Describe the morphology of the red blood cells.
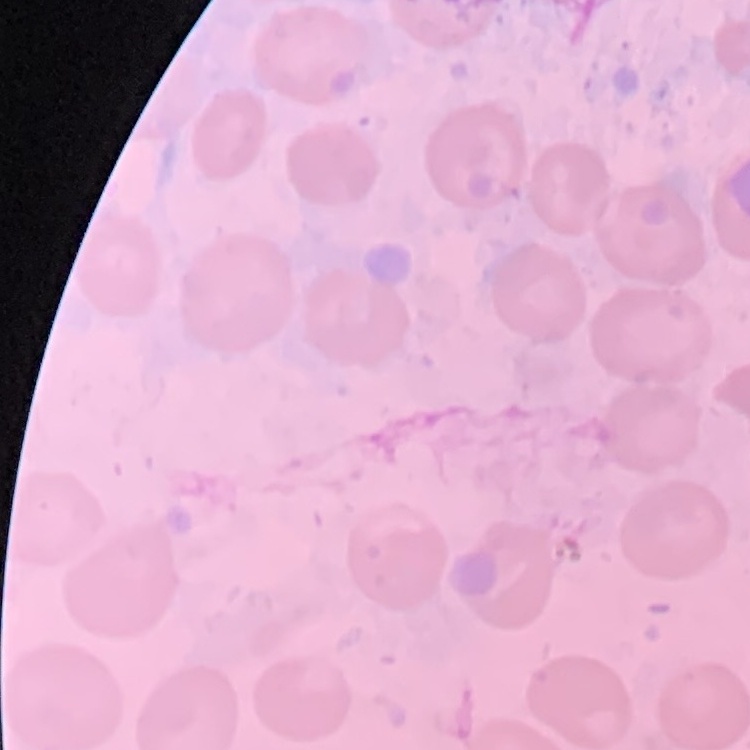
No rouleaux formation.

Summary:
  - Preparation: thin peripheral smear
  - Stain: Field's or Giemsa
  - Image type: square crop of a larger photomicrograph